Describe the morphology of the erythrocytes.
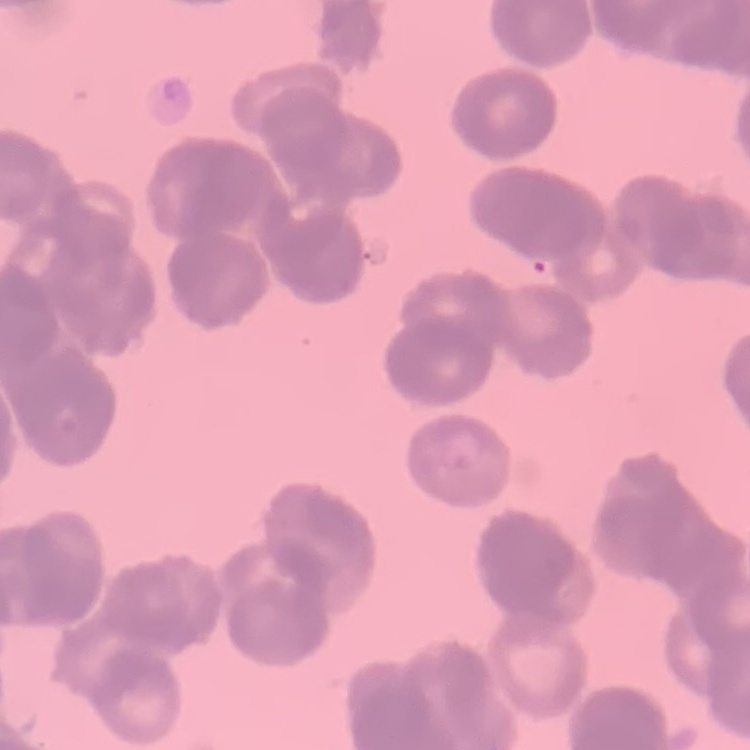
Rouleaux formation.

image_type: square crop of a larger photomicrograph
preparation: thin peripheral smear
stain: Field's or Giemsa